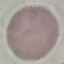

Summary:
  - Malaria status: uninfected
  - Capture: smartphone through the microscope eyepiece
  - Image type: automatically extracted cell patch, resized to 64 × 64 pixels
  - Preparation: thin blood smear
  - Stain: Giemsa